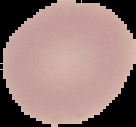

Image is 136×127 pixels. Result: no Plasmodium parasites seen. From a thin blood smear. Segmented cell region on a black background.